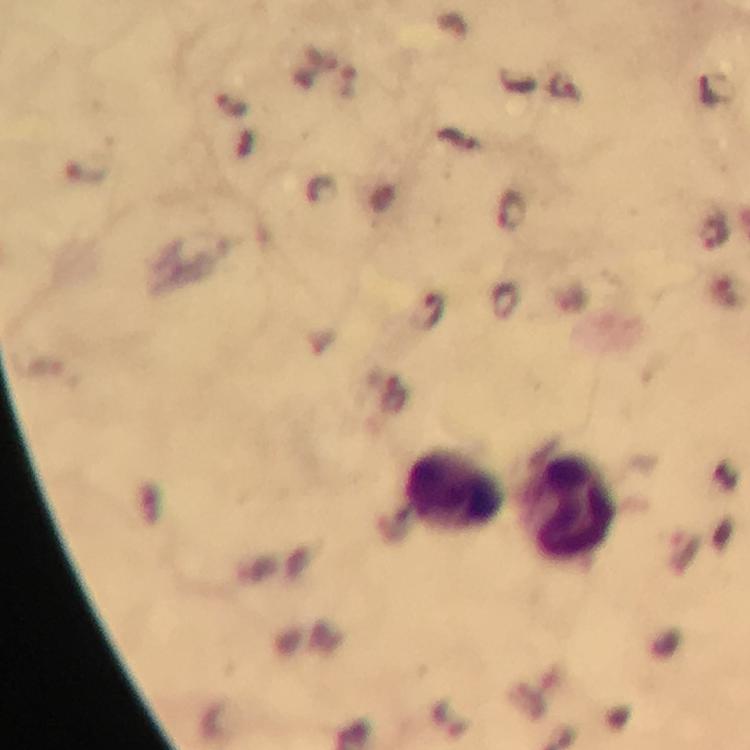
{
  "capture": "smartphone mounted on the microscope",
  "preparation": "thick smear",
  "stain": "Giemsa",
  "leukocyte_locations": "approximate centers as (x, y) in pixels: (452, 490), (563, 506)",
  "image_size": "750×750 pixels",
  "magnification": "100x",
  "context": "from a malaria diagnostic workup",
  "plasmodium_parasite_locations": "approximate centers as (x, y) in pixels: (321, 190), (511, 210), (714, 233), (428, 311)",
  "cropped_from": "one field of view",
  "immersion_oil": "used"
}